Identify the parasite.
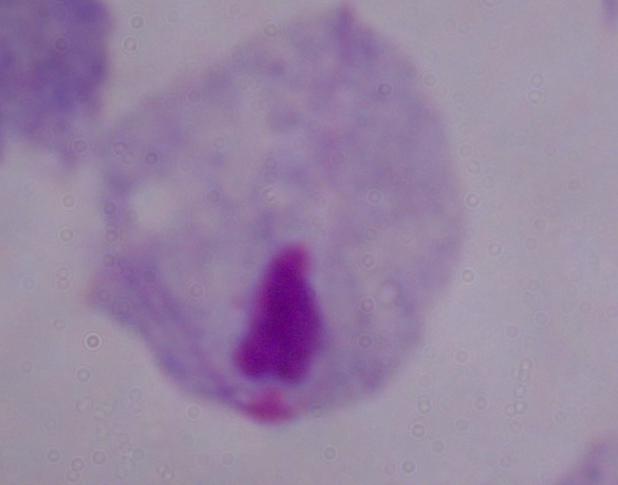

This is a trichomonad.

Summary:
  - Magnification: 1000x
  - Modality: photomicrograph